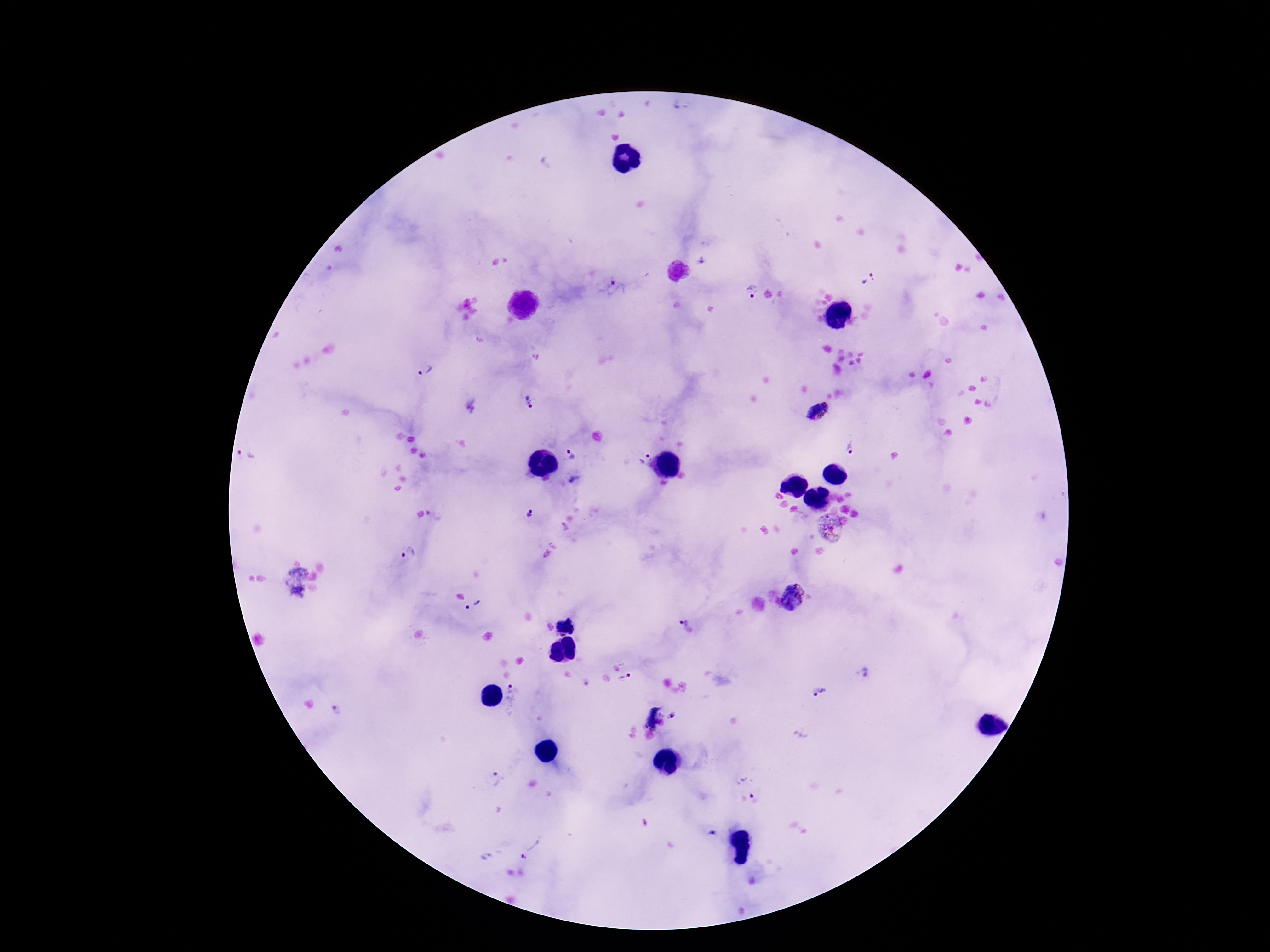 Approximate centers as [x, y] in pixels. Plasmodium parasite locations: [867, 279], [613, 284], [751, 291], [426, 370], [528, 401], [472, 406], [818, 411], [852, 447], [572, 454], [641, 455], [247, 456], [529, 515], [830, 528], [409, 553], [293, 581], [794, 597], [475, 605], [682, 622], [567, 626], [865, 672], [626, 679], [818, 691], [522, 696], [338, 711], [649, 716], [673, 716], [496, 779], [751, 796], [712, 833], [533, 847]. Photographed through the microscope eyepiece with a smartphone camera. 100x magnification. Thick peripheral-blood smear. One field from this slide. Image is 1270×952 pixels. Patient malaria status: infected. Giemsa-stained preparation.